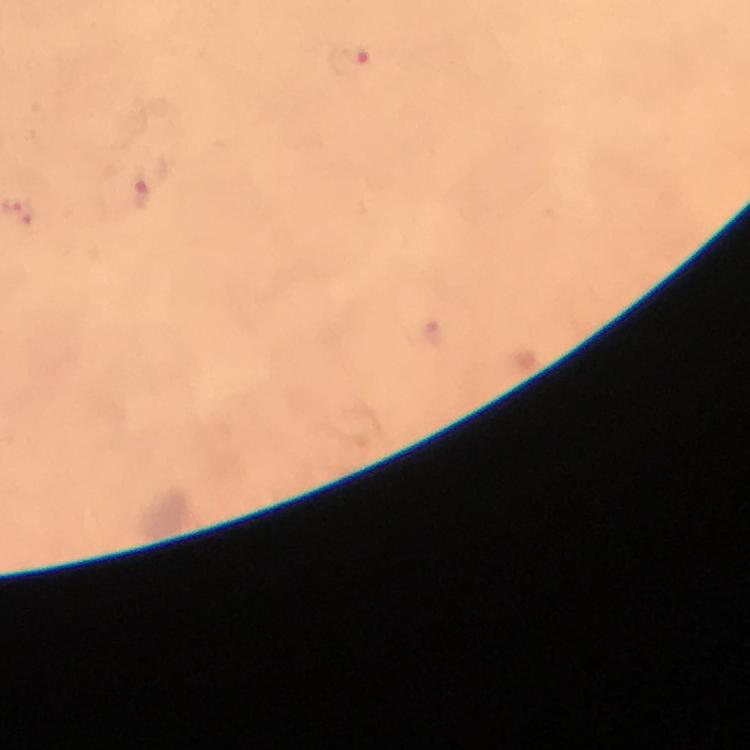

preparation = thick blood film
immersion oil = applied
cropped from = a single field of view
magnification = 100x
context = from a malaria diagnostic workup
malaria parasite locations = approximate object centers, in pixels from the top-left corner: (x=350, y=61), (x=142, y=186)
image size = 750×750 pixels
capture = smartphone photograph through a microscope
stain = Giemsa